Report the malaria status of this cell.
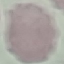
It is uninfected.

Cell patch, automatically extracted from a larger field of view and resized to 64 × 64 pixels. Giemsa-stained preparation. Thin blood smear. Photographed with a smartphone camera at the microscope eyepiece.